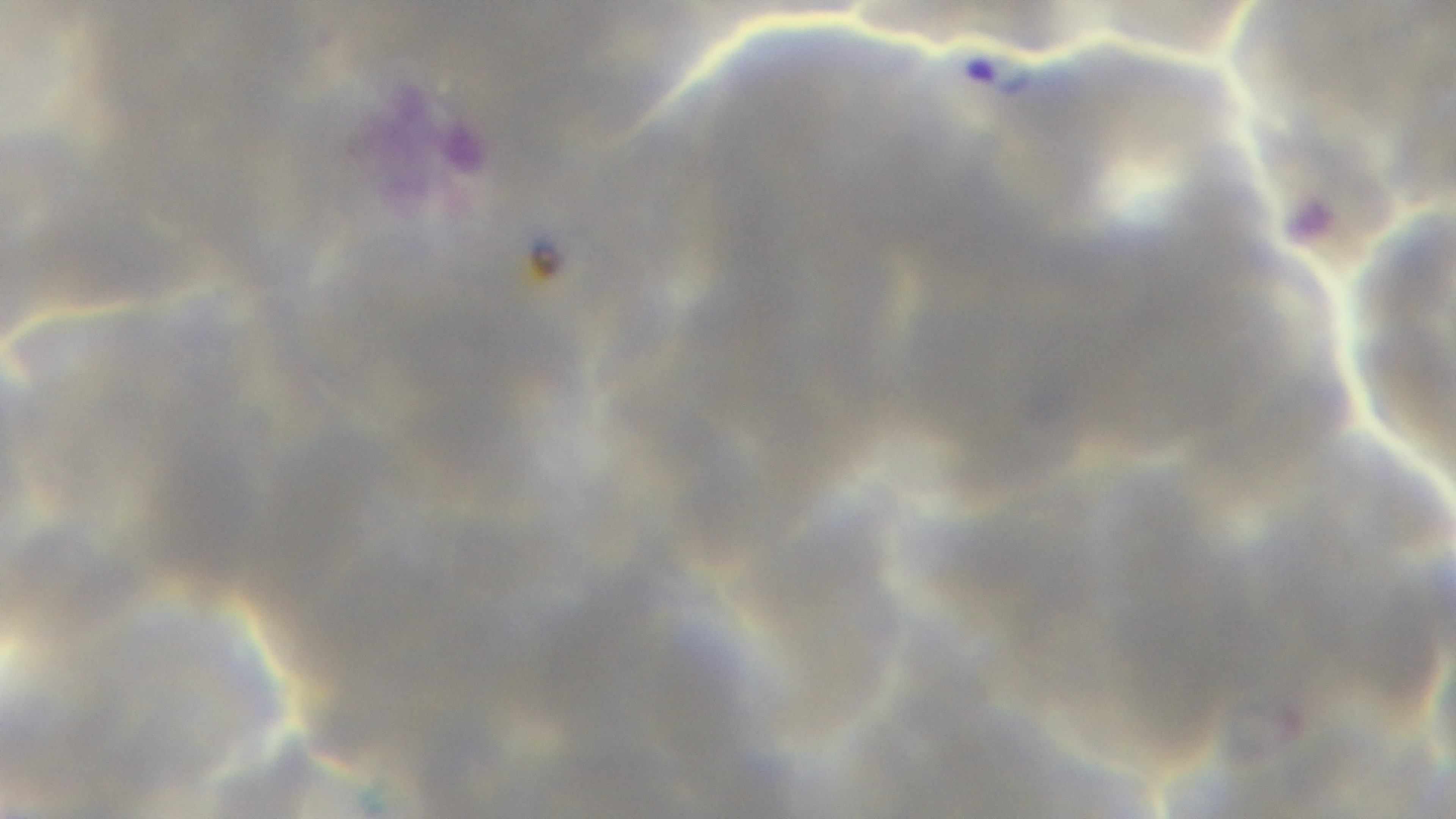
{
  "preparation": "thin",
  "capture": "mounted 4K digital camera",
  "malaria_status": "positive",
  "field_of_view": "single",
  "modality": "light microscopy",
  "stain": "Giemsa",
  "objective": "100x oil immersion"
}